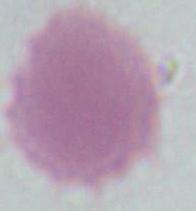
Summary:
  - Magnification: 1000x
  - Identification: red blood cell
  - Modality: micrograph